Describe the morphology of the red blood cells.
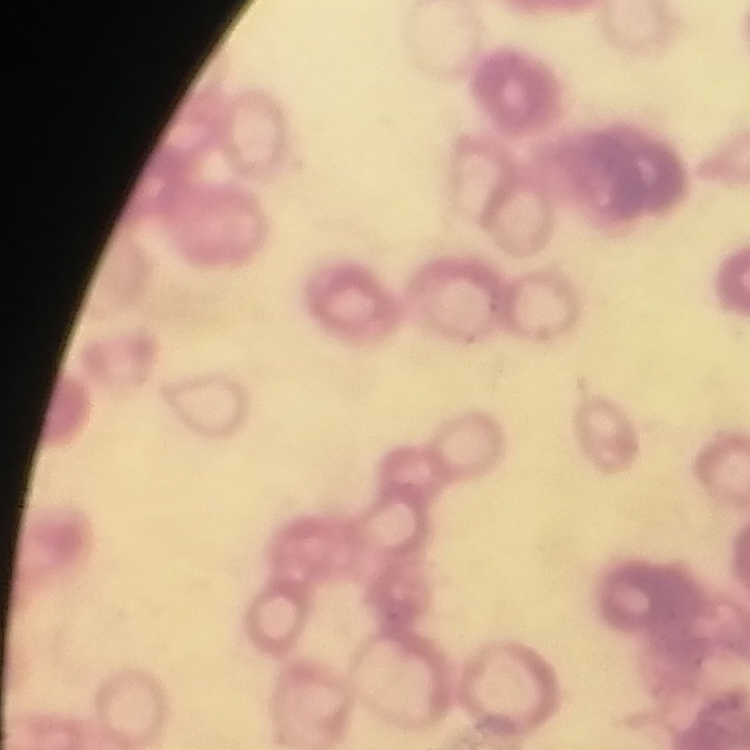

Rouleaux formation.

Thin blood film. Stained with either Field's or Giemsa. One tile cut from a larger photomicrograph.